Report the malaria status.
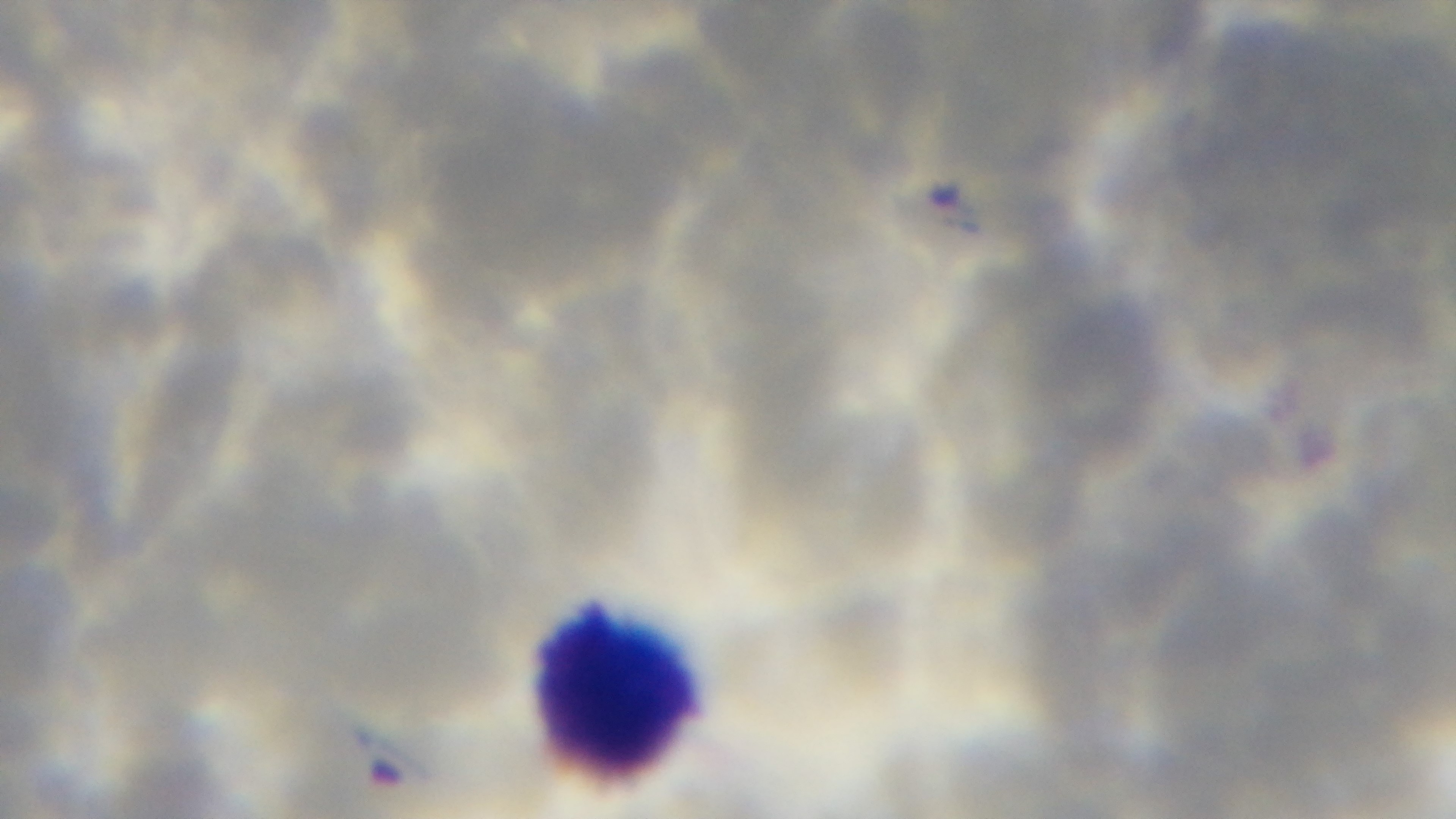

It is infected.

Giemsa-stained. Single field of view. Oil-immersion objective, 100x. Preparation: thin. Photomicrograph. Captured with a mounted 4K digital camera.